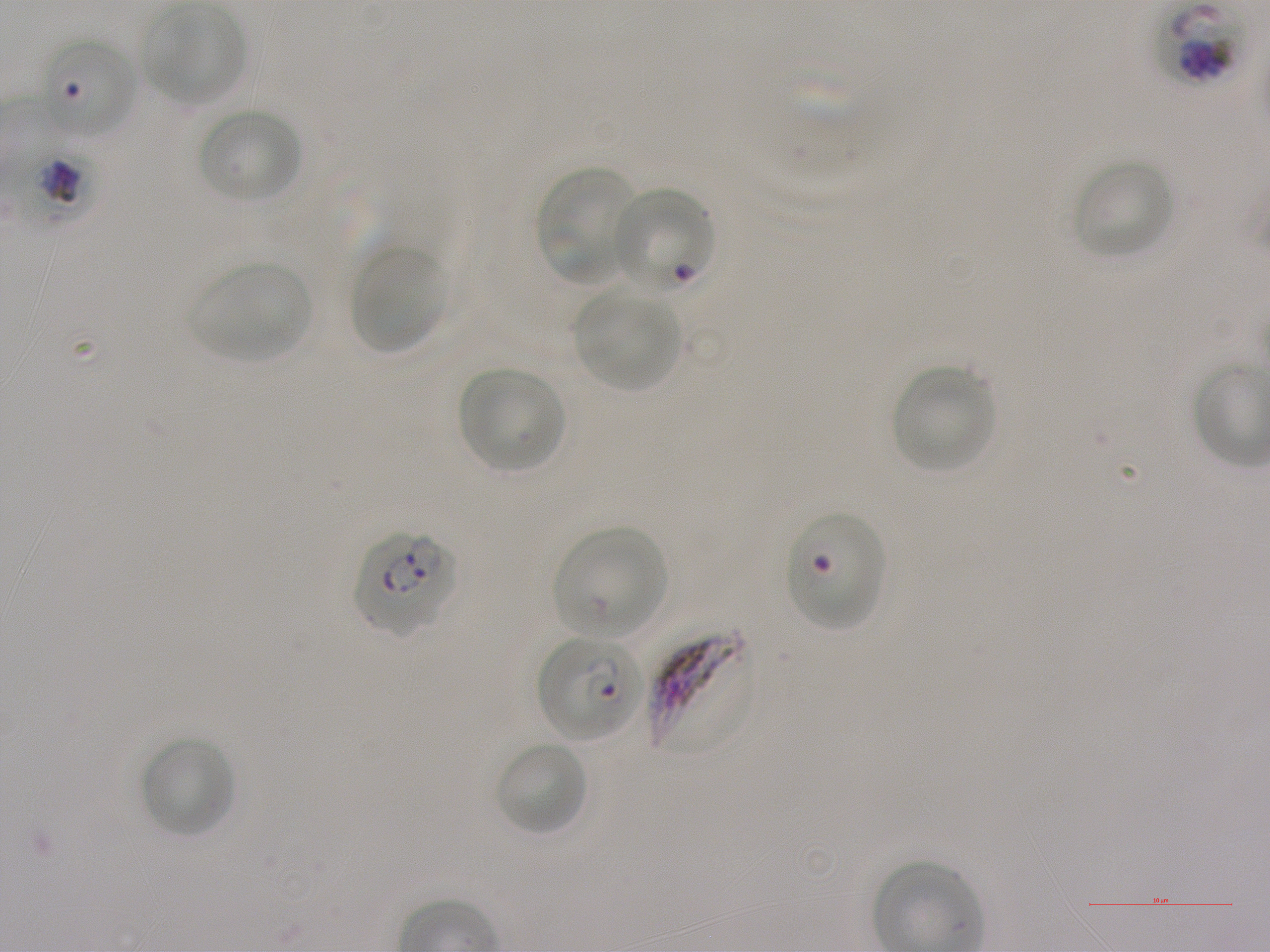
Approximate bounding boxes as {x1, y1, x2, y2} in pixels. Not every red blood cell is marked. A life-cycle stage — or a range of stages, where the recorded stages span more than one — follows each staged infected red blood cell. Locations of infected red blood cells: {1158, 4, 1243, 84}; {12, 140, 103, 231} trophozoite; {610, 186, 716, 296}; {352, 530, 458, 636} ring; {647, 625, 755, 758}; {538, 636, 642, 742} ring. Locations of uninfected red blood cells: {144, 4, 245, 105}, {38, 35, 136, 140}, {194, 108, 305, 204}, {1071, 158, 1174, 260}, {535, 167, 637, 284}, {350, 245, 446, 354}, {191, 260, 312, 362}, {574, 291, 680, 390}, {457, 366, 566, 472}, {891, 366, 997, 474}, {552, 527, 668, 639}, {140, 735, 236, 838}, {495, 740, 588, 836}. Locations of red blood cells of indeterminate infection status: {785, 511, 884, 630}. Life-cycle stages observed: ring, trophozoite. Thin blood smear. Blood group of the donor: A+. 100x objective under oil immersion, numerical aperture 1.25. P. falciparum strain NF54 in static in-vitro culture. Image is 1270×952 pixels. Giemsa stain. One field from this slide.